Assess for malaria.
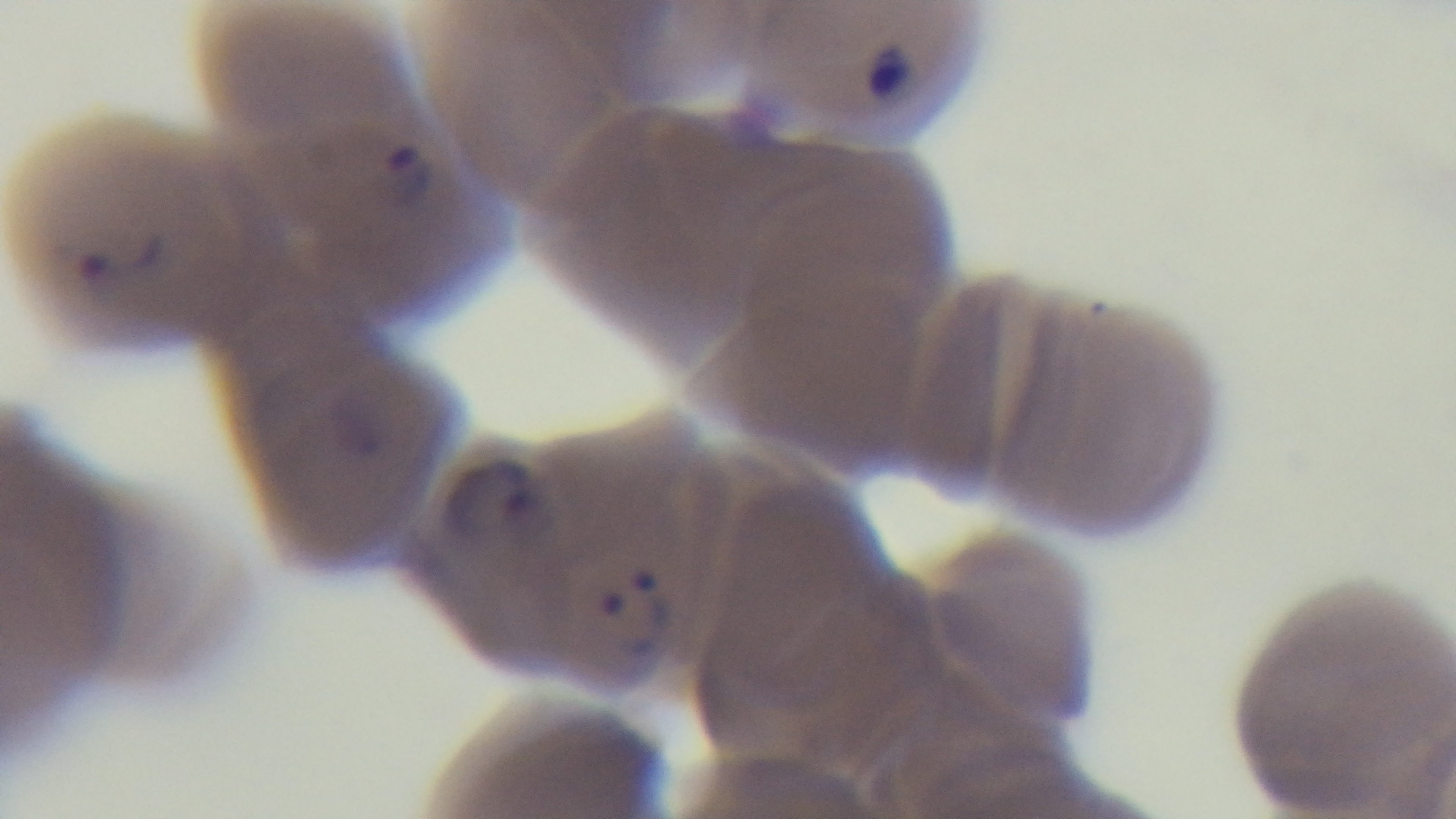

Infected.

Preparation: thin. Mounted 4K digital camera. One field from the slide. Photomicrograph. Giemsa stain. 100x oil-immersion objective.